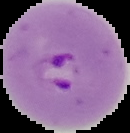 Image is 130×133 pixels. From a thin blood smear. The area outside the segmented cell region is set to black. Malaria status: parasitized.